Outline each blood parasite and name the species.
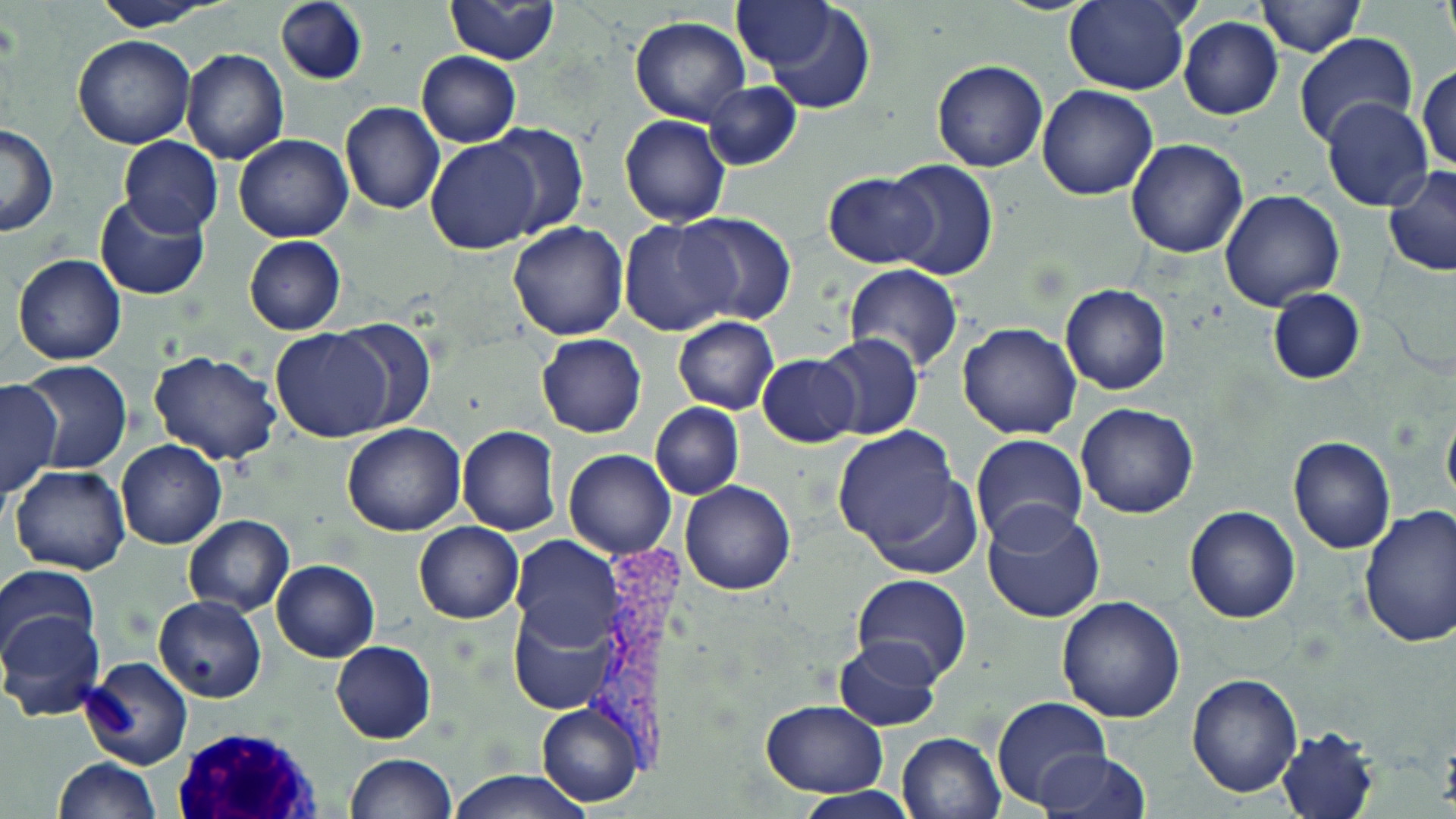

Approximate bounding boxes as (x1,y1)-(x2,y2) corner pairs in pixels.
Plasmodium vivax-infected red blood cells: (589,535)-(686,783).
No Plasmodium falciparum, Plasmodium ovale, Plasmodium malariae, Babesia divergens, or Trypanosoma brucei observed.

White blood cell locations: (171,725)-(322,818). Uninfected red blood cell locations: (89,0)-(224,31), (446,0)-(560,66), (1439,0)-(1454,55), (276,1)-(367,84), (757,1)-(878,114), (1063,1)-(1192,93), (1257,1)-(1364,57), (733,2)-(837,71), (629,17)-(751,126), (1179,17)-(1284,120), (71,34)-(196,148), (1294,34)-(1419,148), (181,49)-(289,165), (416,51)-(520,147), (931,59)-(1049,172), (1416,64)-(1455,173), (702,81)-(801,171), (1037,85)-(1158,200), (1321,97)-(1433,213), (340,103)-(446,216), (619,113)-(731,228), (480,123)-(588,240), (0,125)-(59,238), (234,133)-(353,242), (117,135)-(223,237), (426,137)-(545,255), (1125,137)-(1250,257), (882,159)-(998,280), (1382,164)-(1456,277), (824,172)-(933,267), (1220,190)-(1345,310), (95,193)-(210,301), (676,211)-(797,325), (617,217)-(737,338), (508,221)-(629,341), (243,235)-(346,335), (12,254)-(125,365), (844,265)-(964,373), (1059,284)-(1171,395), (1266,288)-(1366,384), (674,317)-(777,413), (325,319)-(439,433), (957,322)-(1083,439), (270,328)-(396,442), (536,334)-(648,438), (814,335)-(924,439), (148,350)-(281,464), (756,356)-(859,446), (19,359)-(132,473), (2,373)-(62,496), (1441,401)-(1456,519), (650,402)-(742,500), (1075,402)-(1198,518), (342,422)-(466,537), (457,425)-(562,537), (832,425)-(973,567), (970,434)-(1089,549), (1288,437)-(1396,554), (115,440)-(228,550), (564,448)-(675,559), (9,465)-(130,575), (679,479)-(795,595), (981,503)-(1107,623), (1184,504)-(1300,622), (1357,506)-(1456,647), (183,514)-(295,616), (414,521)-(523,624), (510,535)-(620,651), (271,559)-(378,662), (1,563)-(100,667), (852,574)-(973,684), (1056,595)-(1185,722), (153,596)-(267,704), (511,599)-(619,715), (2,609)-(105,721), (832,638)-(943,731), (330,640)-(436,743), (81,656)-(194,770), (1187,672)-(1303,795), (990,695)-(1111,810), (758,699)-(888,797), (536,701)-(644,807), (1276,726)-(1380,819), (896,732)-(1005,819), (1034,748)-(1151,818), (344,754)-(455,818), (54,757)-(160,818), (446,771)-(589,819), (792,787)-(919,818). Slide-level diagnosis: Plasmodium vivax. Thin blood smear. Single field of view. Captured at 1000x magnification. Light microscopy. May-Grünwald-Giemsa-stained preparation. Image is 1456×819 pixels.